Report the malaria status of this cell.
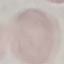

Uninfected.

Photographed with a smartphone camera at the microscope eyepiece. Giemsa stain. Thin smear of blood. Automatically extracted cell patch, resized to 64 × 64 pixels.